Classify this cell by malaria status.
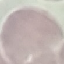
Uninfected.

image_type: cell patch, automatically extracted from a larger field of view and resized to 64 × 64 pixels
stain: Giemsa
preparation: thin smear
capture: smartphone camera at the microscope eyepiece